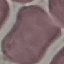
Malaria status: uninfected. Automatically extracted cell patch, resized to 64 × 64 pixels. Thin blood smear. Giemsa-stained preparation. Photographed with a smartphone camera at the microscope eyepiece.